Name the cell type shown.
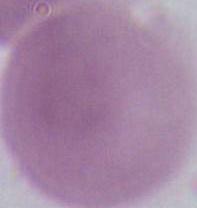
An erythrocyte.

modality: micrograph
magnification: 1000x